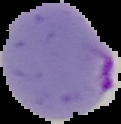 Image is 121×124 pixels. Malaria status: parasitized. From a thin blood film. Cell region segmented out of the field of view; the surrounding area is masked to black.